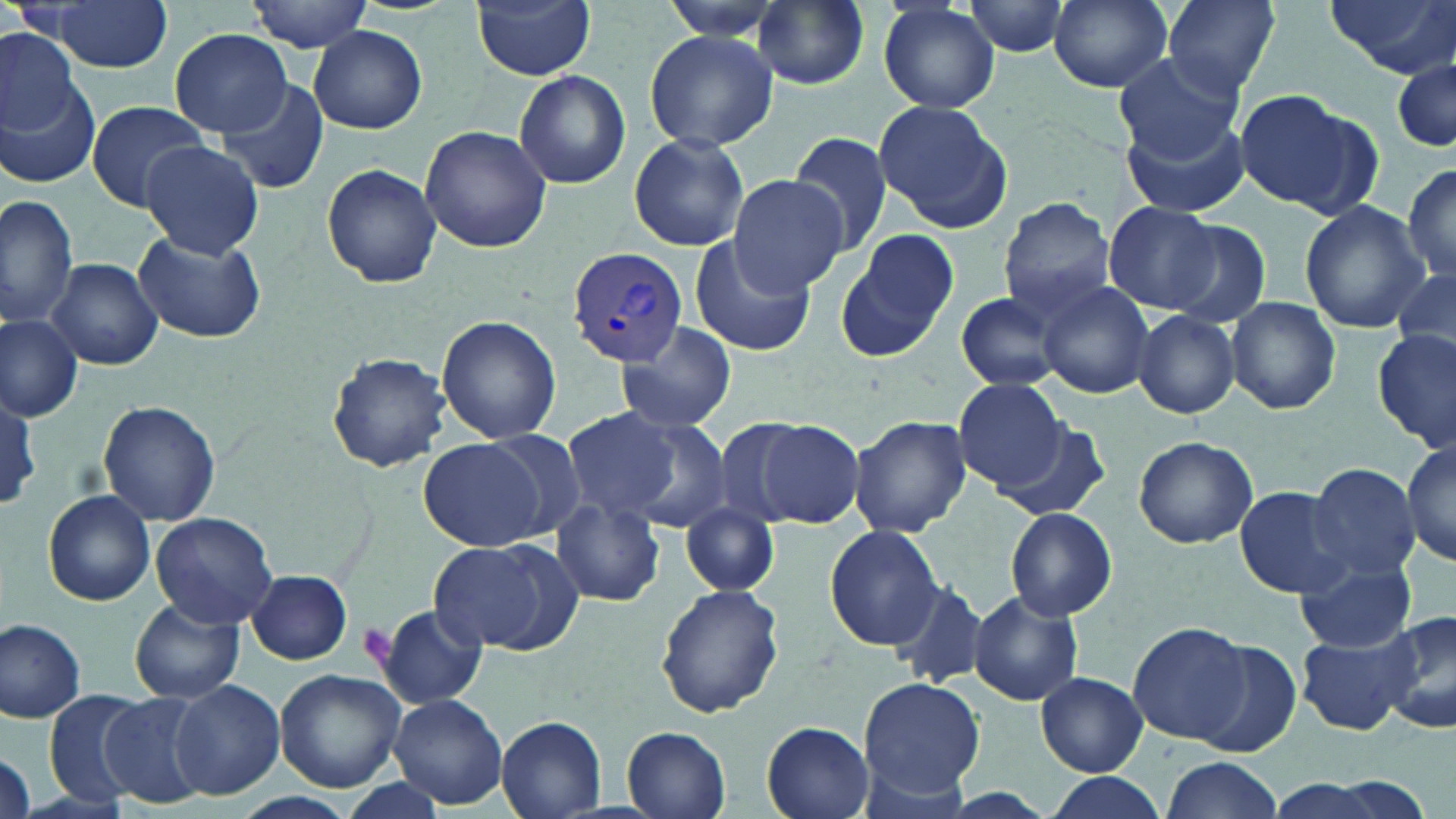
Summary:
  - Coordinate format: approximate bounding boxes as [x1, y1, x2, y2] in pixels
  - Uninfected red blood cell locations: [48, 0, 173, 71], [246, 0, 374, 52], [472, 0, 595, 80], [659, 0, 787, 38], [753, 0, 869, 89], [878, 0, 1000, 113], [962, 0, 1073, 57], [1048, 0, 1175, 91], [1323, 0, 1455, 77], [1162, 1, 1280, 96], [310, 26, 426, 133], [168, 29, 295, 136], [645, 29, 777, 152], [0, 31, 81, 137], [1112, 50, 1244, 162], [1392, 55, 1454, 155], [513, 69, 631, 189], [1, 72, 102, 190], [216, 76, 330, 195], [1234, 89, 1362, 210], [873, 100, 1012, 232], [86, 101, 210, 211], [1122, 111, 1251, 217], [419, 126, 552, 251], [785, 129, 897, 261], [628, 134, 749, 253], [140, 140, 263, 259], [1404, 162, 1456, 285], [322, 163, 441, 286], [727, 176, 848, 295], [0, 193, 78, 332], [998, 197, 1117, 319], [1299, 199, 1429, 333], [1104, 202, 1219, 312], [1156, 218, 1272, 328], [840, 228, 958, 358], [134, 231, 264, 343], [688, 234, 813, 357], [47, 257, 161, 368], [1392, 265, 1456, 365], [1039, 281, 1154, 399], [955, 292, 1062, 391], [1228, 296, 1340, 415], [1133, 310, 1240, 419], [1, 314, 83, 421], [436, 314, 562, 445], [616, 321, 736, 434], [1373, 328, 1455, 450], [327, 353, 450, 469], [954, 377, 1065, 492], [1, 389, 43, 510], [96, 400, 221, 527], [560, 408, 685, 523], [607, 412, 733, 532], [846, 414, 971, 537], [708, 415, 817, 532], [751, 418, 866, 529], [993, 419, 1112, 522], [1134, 435, 1258, 548], [418, 438, 551, 551], [1400, 441, 1455, 567], [1305, 463, 1421, 579], [1234, 485, 1355, 598], [42, 489, 156, 606], [550, 497, 665, 606], [681, 502, 778, 596], [1004, 507, 1118, 620], [150, 511, 279, 627], [824, 524, 946, 650], [426, 537, 578, 656], [1296, 559, 1417, 653], [247, 569, 352, 664], [888, 582, 986, 690], [656, 583, 783, 719], [969, 590, 1084, 707], [132, 595, 244, 705], [374, 605, 486, 709], [1379, 609, 1456, 739], [1, 617, 86, 720], [1128, 622, 1254, 746], [1296, 630, 1419, 736], [1191, 641, 1303, 760], [275, 669, 406, 790], [1037, 672, 1146, 776], [858, 678, 985, 799], [169, 680, 284, 802], [97, 690, 216, 809], [44, 691, 147, 806], [389, 692, 507, 809], [496, 715, 607, 818], [761, 722, 874, 818], [623, 727, 732, 818], [0, 746, 37, 819], [1157, 757, 1285, 818], [1040, 773, 1166, 819], [228, 792, 360, 819]
  - Plasmodium vivax-infected red blood cell locations: [566, 247, 691, 365]
  - Platelet locations: [357, 623, 395, 666]
  - Slide-level diagnosis: Plasmodium vivax
  - Stain: May-Grünwald-Giemsa
  - Image size: 1456×819 pixels
  - Magnification: 1000x
  - Field of view: one of a larger specimen
  - Modality: light microscopy
  - Preparation: thin blood film